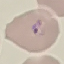

Result: malaria parasites detected. Thin smear of blood. Automatically extracted cell patch, resized to 64 × 64 pixels. Giemsa-stained preparation. Acquired by smartphone through the microscope eyepiece.